Assess the morphology of the erythrocytes.
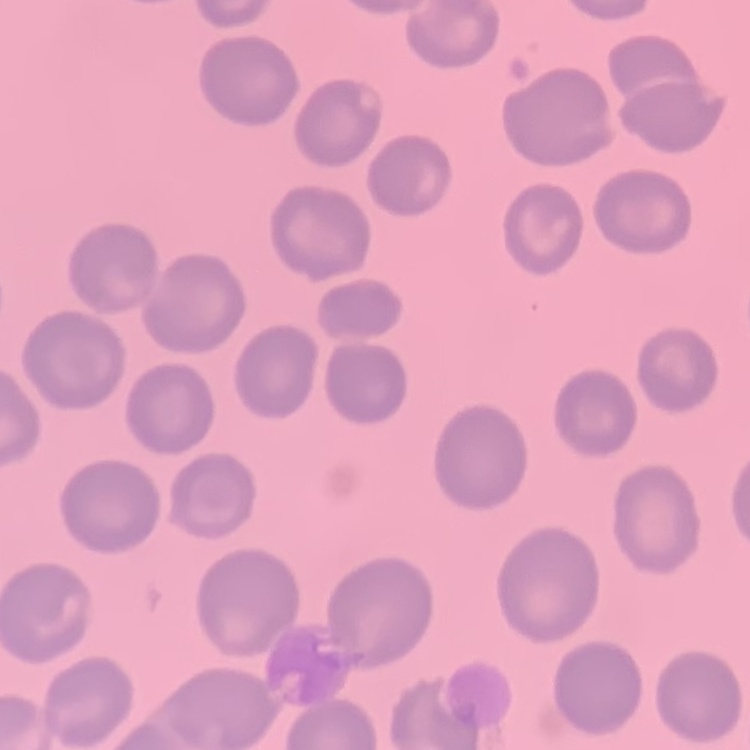

No rouleaux formation.

{
  "stain": "Field's or Giemsa",
  "preparation": "thin blood smear",
  "image_type": "one tile cut from a larger photomicrograph"
}